Classify this cell by malaria status.
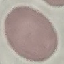

It is uninfected.

{
  "image_type": "cell patch, automatically extracted from a larger field of view and resized to 64 × 64 pixels",
  "preparation": "thin blood smear",
  "stain": "Giemsa",
  "capture": "smartphone camera at the microscope eyepiece"
}